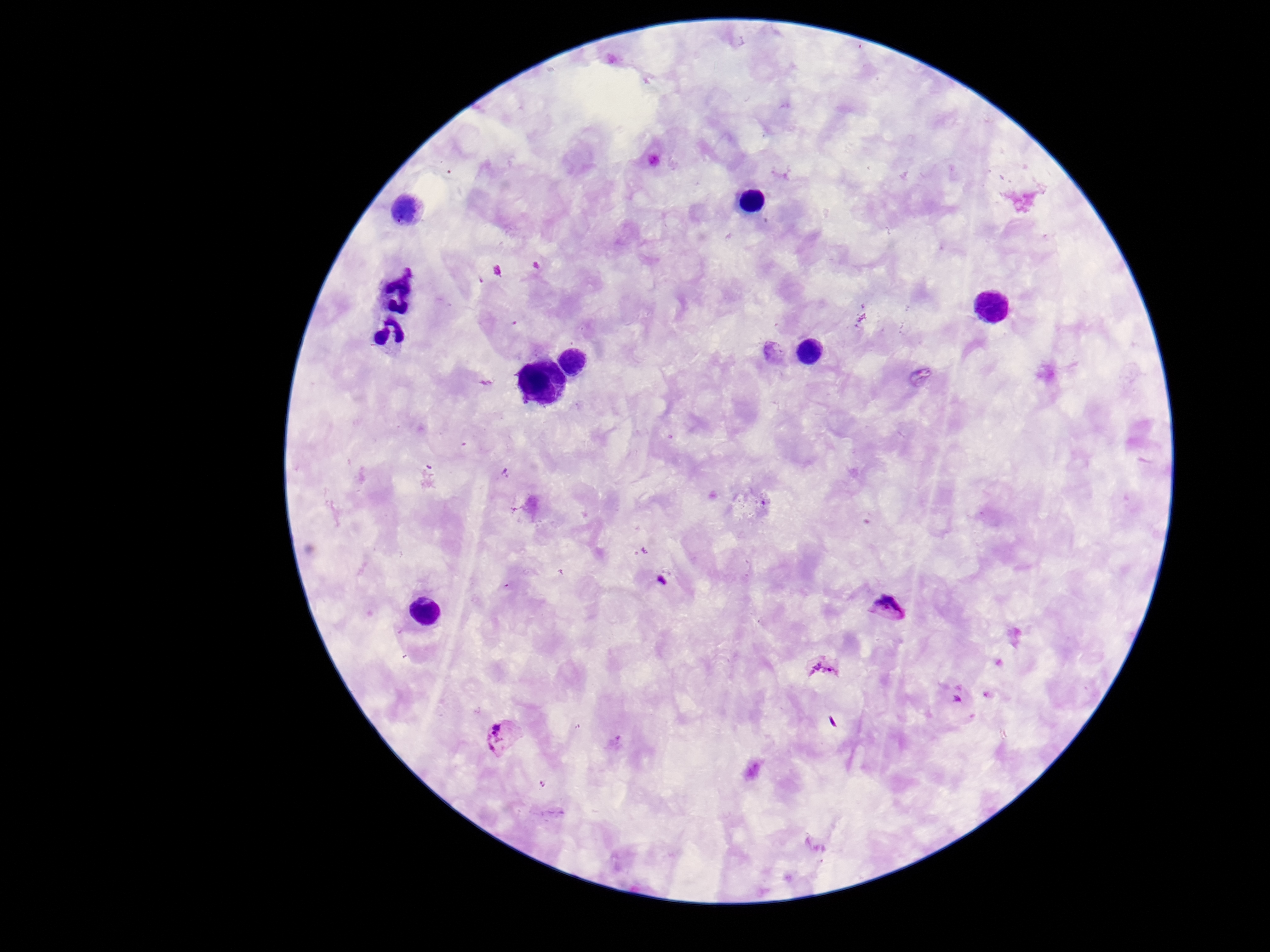
image_size: 1270×952 pixels
preparation: thick blood smear
plasmodium_parasite_locations: 'approximate centers as [x, y] in pixels: [774, 355], [891, 608], [825, 669], [500, 733]'
stain: Giemsa
magnification: 100x
field_of_view: one from this slide
capture: smartphone camera through the microscope eyepiece
patient_malaria_status: infected